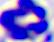
Summary:
  - Modality: micrograph
  - Magnification: 400x
  - Identification: leukocyte